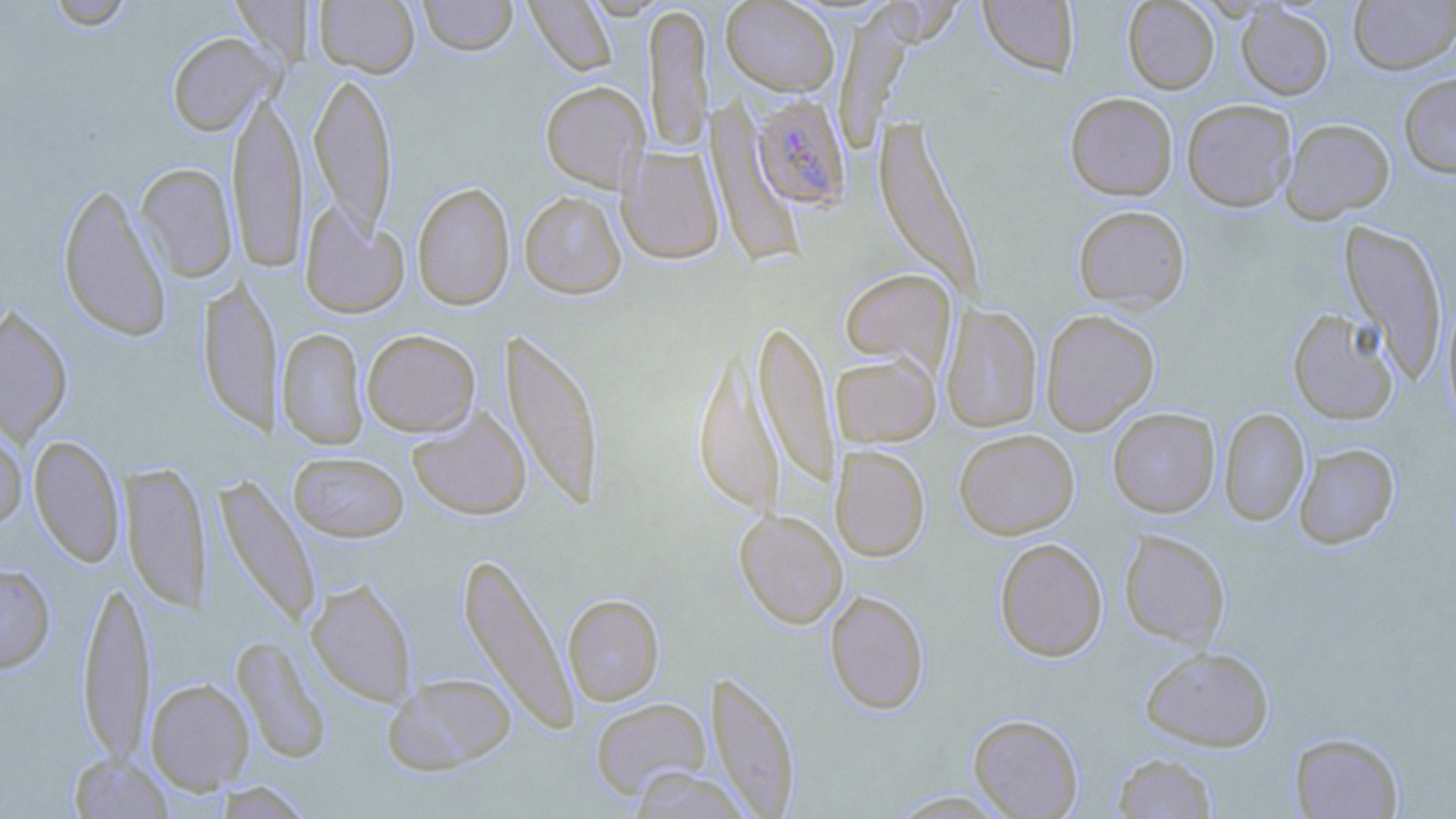
{
  "plasmodium_falciparum_infected_red_blood_cell_locations": "approximate bounding boxes as (x1,y1)-(x2,y2) corner pairs in pixels: (751,93)-(850,209)",
  "slide_level_diagnosis": "Plasmodium falciparum",
  "field_of_view": "single",
  "modality": "light microscopy",
  "stain": "May-Grünwald-Giemsa",
  "preparation": "thin blood smear",
  "magnification": "1000x",
  "image_size": "1456×819 pixels",
  "uninfected_red_blood_cell_locations": "approximate bounding boxes as (x1,y1)-(x2,y2) corner pairs in pixels: (46,0)-(134,29), (314,0)-(420,78), (417,0)-(518,56), (524,0)-(617,76), (1122,0)-(1219,94), (721,1)-(839,96), (979,1)-(1078,77), (1348,1)-(1456,74), (643,3)-(712,154), (1236,3)-(1334,100), (167,32)-(277,136), (309,71)-(397,237), (1399,71)-(1456,178), (541,81)-(650,192), (227,88)-(307,273), (1065,92)-(1177,200), (1181,98)-(1297,211), (706,99)-(806,267), (875,117)-(981,294), (1281,118)-(1395,222), (619,146)-(725,263), (135,163)-(238,281), (58,182)-(171,342), (412,182)-(515,310), (519,191)-(626,299), (300,203)-(409,319), (1073,205)-(1190,312), (1340,219)-(1448,382), (840,268)-(956,373), (198,276)-(281,436), (1442,299)-(1456,429), (0,305)-(73,444), (941,305)-(1042,433), (1040,309)-(1159,435), (1288,309)-(1399,425), (755,319)-(839,491), (278,328)-(368,449), (501,328)-(605,511), (362,329)-(480,437), (693,344)-(782,519), (831,353)-(940,447), (1219,407)-(1309,526), (1108,408)-(1220,517), (407,409)-(531,520), (0,424)-(28,531), (954,429)-(1079,539), (29,435)-(125,566), (1293,443)-(1399,549), (831,444)-(930,561), (289,451)-(409,542), (120,462)-(211,610), (212,474)-(322,629), (735,510)-(848,628), (1119,529)-(1230,648), (994,537)-(1107,661), (458,551)-(579,734), (0,563)-(56,673), (77,574)-(155,766), (307,578)-(418,706), (824,590)-(929,714), (563,594)-(664,705), (232,636)-(331,764), (1140,647)-(1274,751), (706,670)-(801,817), (383,672)-(517,774), (146,678)-(254,793), (589,698)-(711,799), (968,713)-(1083,818), (1290,732)-(1403,818), (68,752)-(173,818), (1112,752)-(1219,818), (626,766)-(753,819), (211,781)-(314,818), (885,790)-(1015,817)"
}